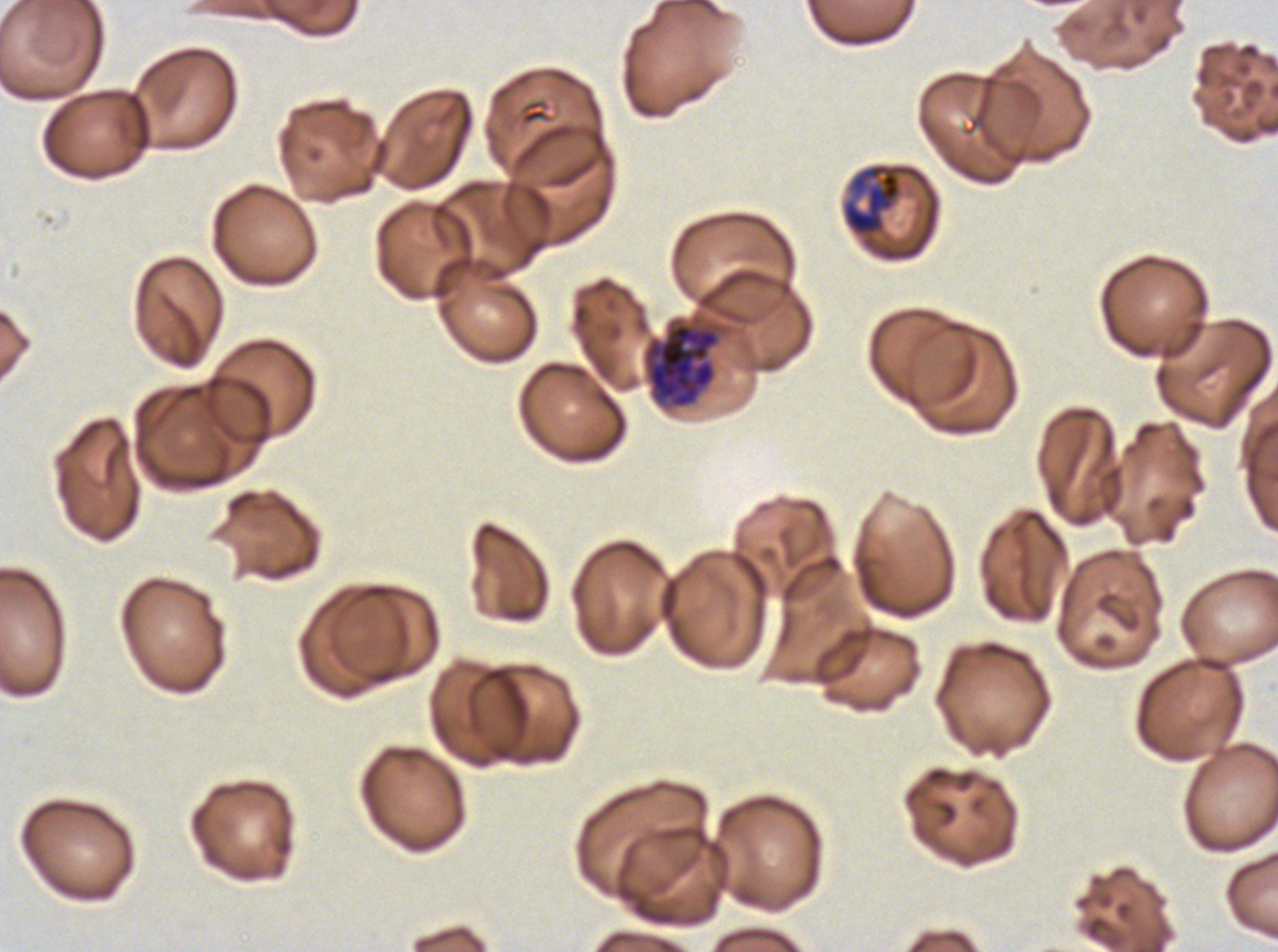
Approximate bounding rectangles given as corner coordinates in pixels from the top-left.
Summary:
  - Late schizont locations: (x1=642, y1=319, x2=721, y2=409)
  - Early schizont locations: (x1=842, y1=164, x2=902, y2=236)
  - Stain: Giemsa
  - Preparation: thin blood smear
  - Specimen: ex-vivo P. falciparum culture from a patient in The Gambia, grown for 24 to 48 hours
  - Life-cycle stages observed: early schizont, late schizont
  - Image size: 1278×952 pixels
  - Field of view: one sub-image of a larger composite